Report the malaria status of this cell.
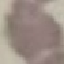
It is uninfected.

Summary:
  - Capture: smartphone through the microscope eyepiece
  - Preparation: thin blood film
  - Image type: automatically extracted cell patch, resized to 64 × 64 pixels
  - Stain: Giemsa